Evaluate for parasitized red blood cells.
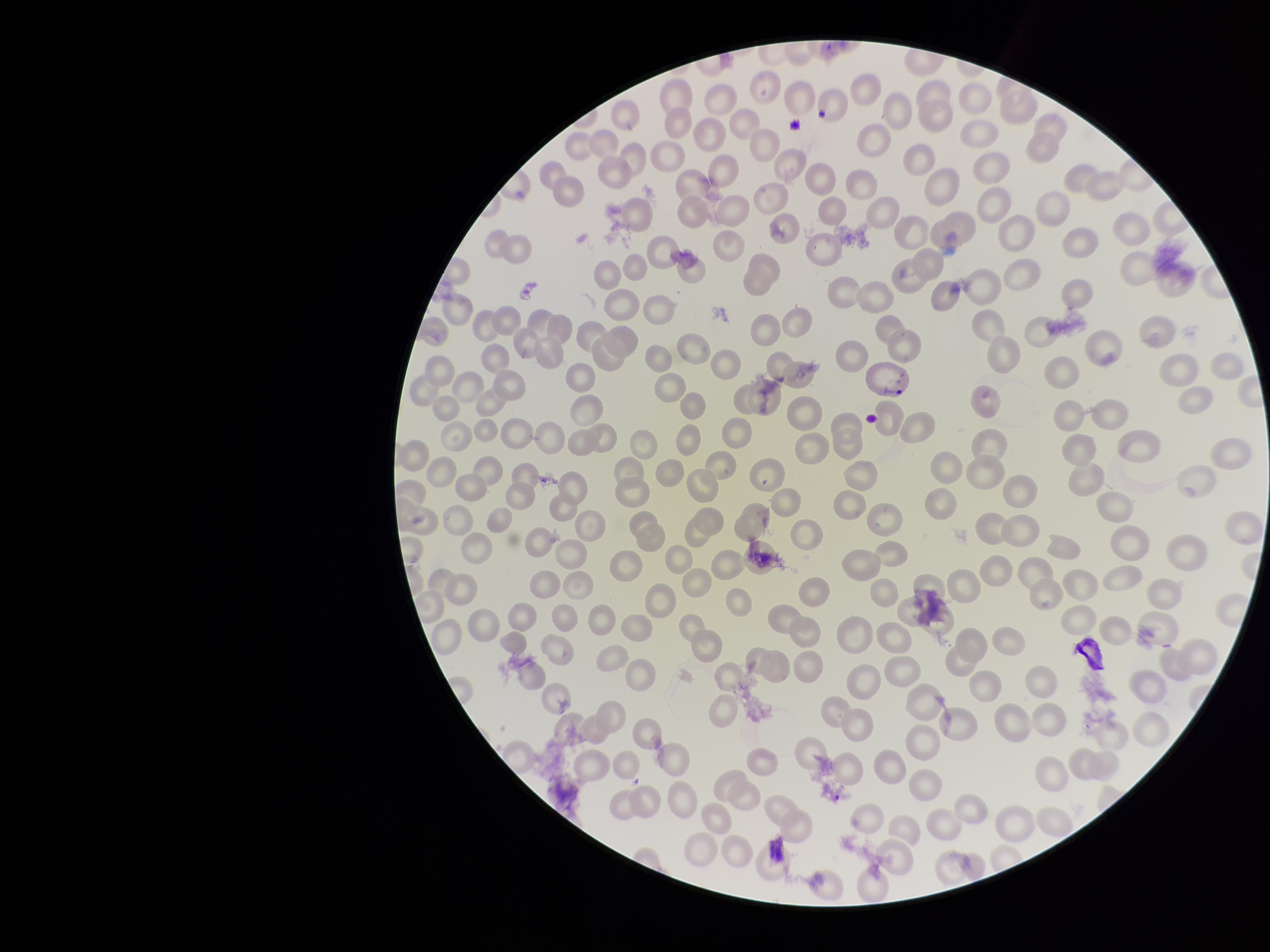
Identified.

Parasitized red blood cell count: 1. Image is 1270×952 pixels. Stained with Giemsa. Preparation: thin. Red blood cell count: 241. Species reported for this patient: Plasmodium vivax. Patient malaria status: infected. Single field of view. Smartphone photograph taken through the eyepiece of a microscope.